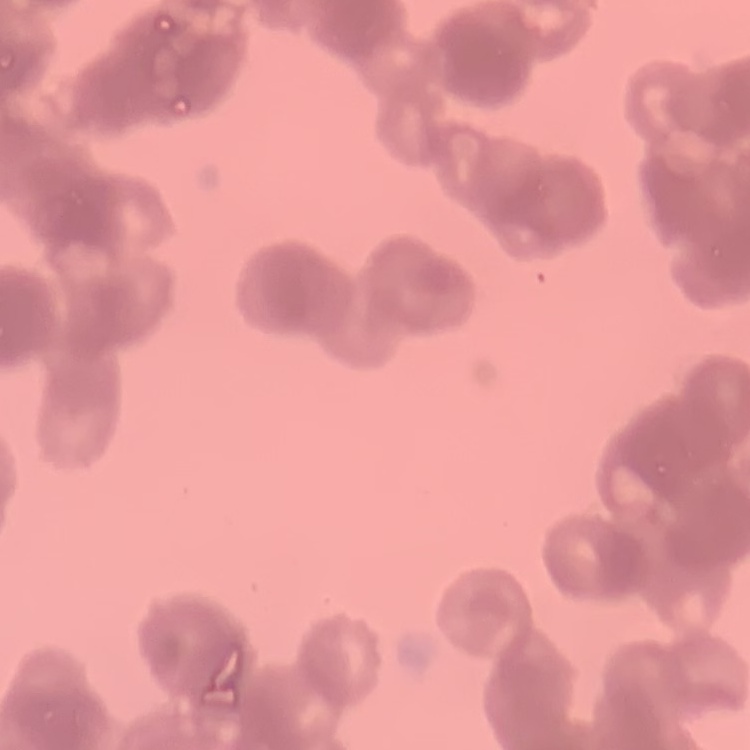 The red blood cells exhibit rouleaux formation. Field's or Giemsa stain. Thin blood film. Square crop of a larger photomicrograph.